Assess this cell for malaria.
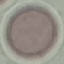
Uninfected.

{
  "capture": "smartphone camera at the microscope eyepiece",
  "image_type": "cell patch, automatically extracted from a larger field of view and resized to 64 × 64 pixels",
  "preparation": "thin blood smear",
  "stain": "Giemsa"
}